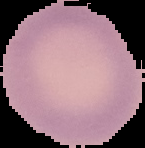 Segmented cell region on a black background. Result: no malaria parasites detected. Image is 145×148 pixels. From a thin blood smear.